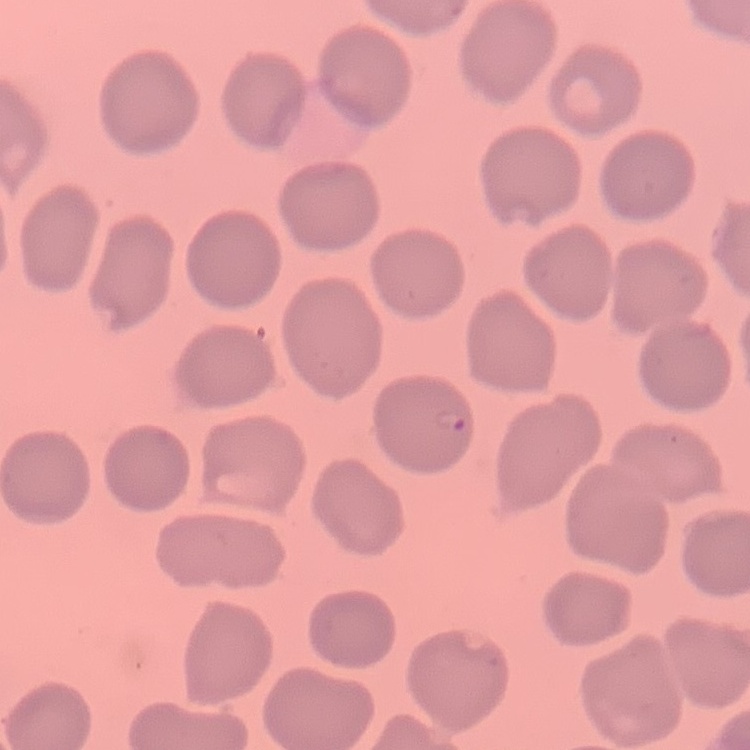

The erythrocytes show no rouleaux formation. Field's or Giemsa stain. One tile cut from a larger photomicrograph. Thin blood smear.